Outline every parasitised red blood cell.
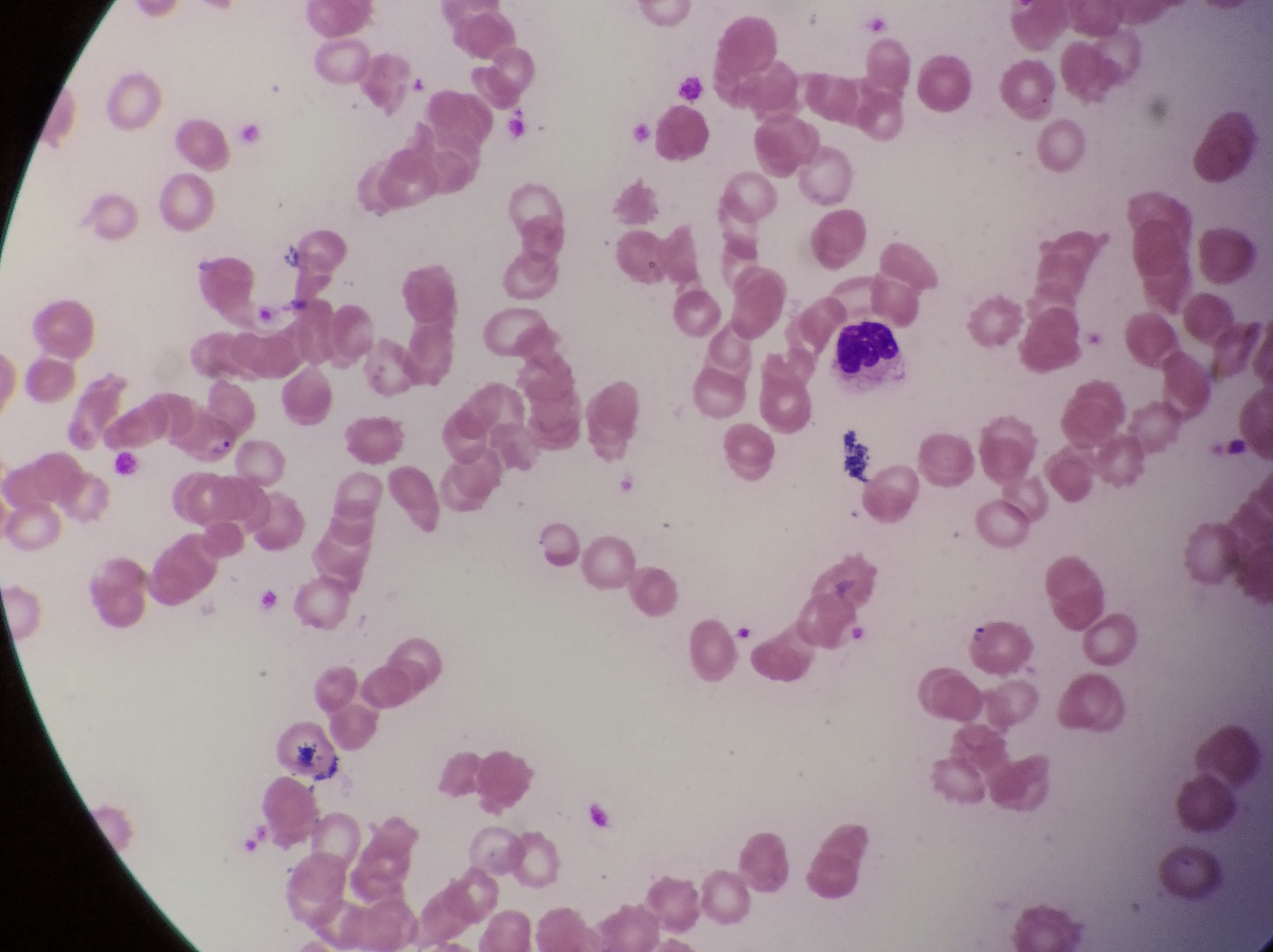

Approximate bounding boxes as (left, top, right, bottom) in pixels.
Parasitised red blood cells: (183, 405, 248, 472).

Leukocyte locations: (834, 323, 908, 385). Photographed through the eyepiece of an Olympus CX-23 microscope with a smartphone camera. Single field of view. Image is 1273×952 pixels. Magnification of 1000x. Thin blood film. Collected in Uganda.